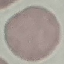 Result: no malaria parasites detected. Giemsa-stained preparation. Thin blood film. Automatically extracted cell patch, resized to 64 × 64 pixels. Photographed with a smartphone camera at the microscope eyepiece.